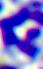

modality = micrograph
identification = white blood cell
magnification = 400x